Evaluate for parasitized red blood cells.
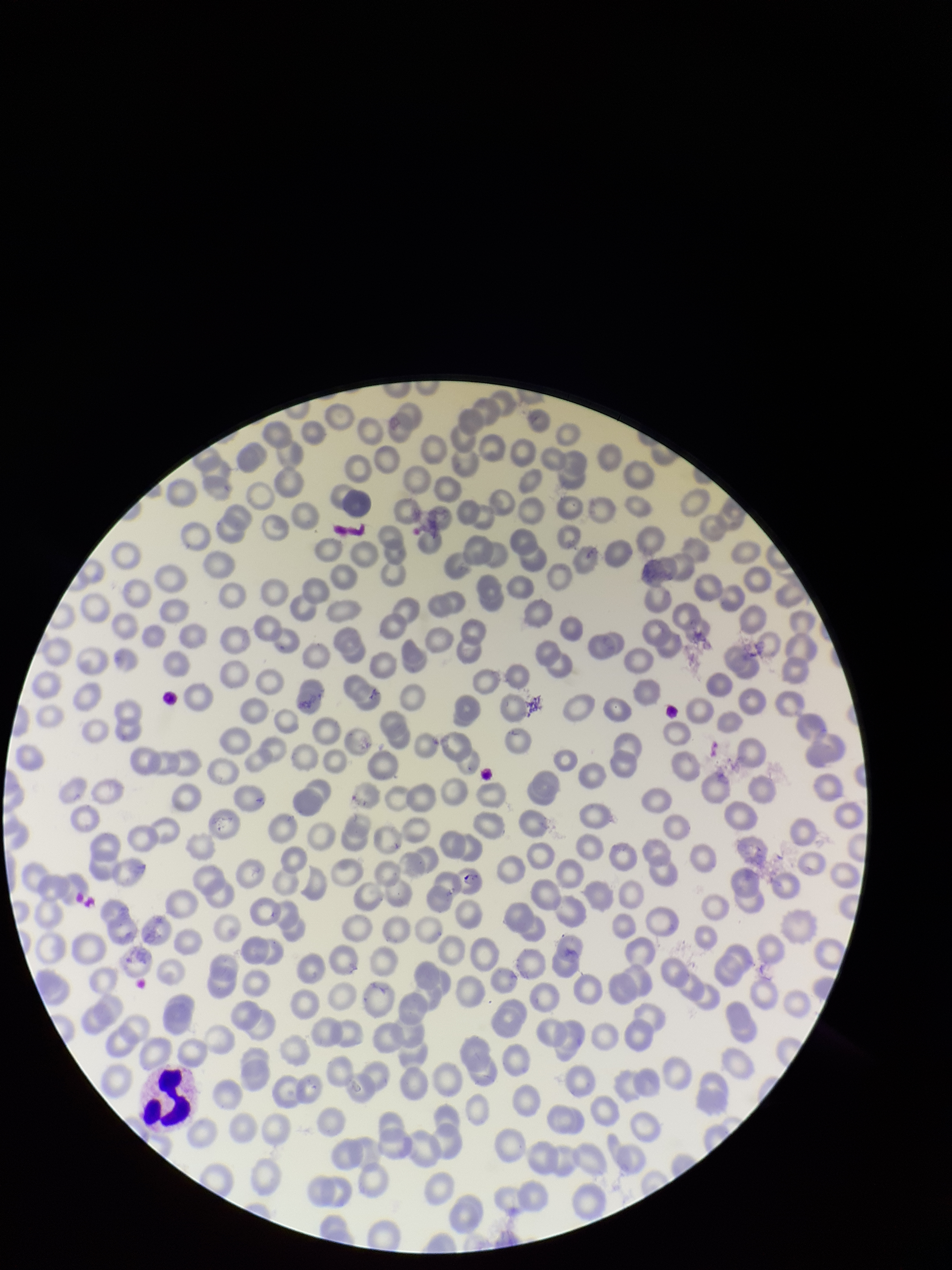
Seen.

Summary:
  - Patient malaria status: positive
  - Parasitized red blood cell count: 1
  - Preparation: thin blood smear
  - Capture: smartphone photograph through the microscope eyepiece
  - Stain: Giemsa
  - Field of view: one from this slide
  - Red blood cell count: 229
  - Image size: 952×1270 pixels
  - Species reported for this patient: Plasmodium falciparum